Outline every Plasmodium parasite.
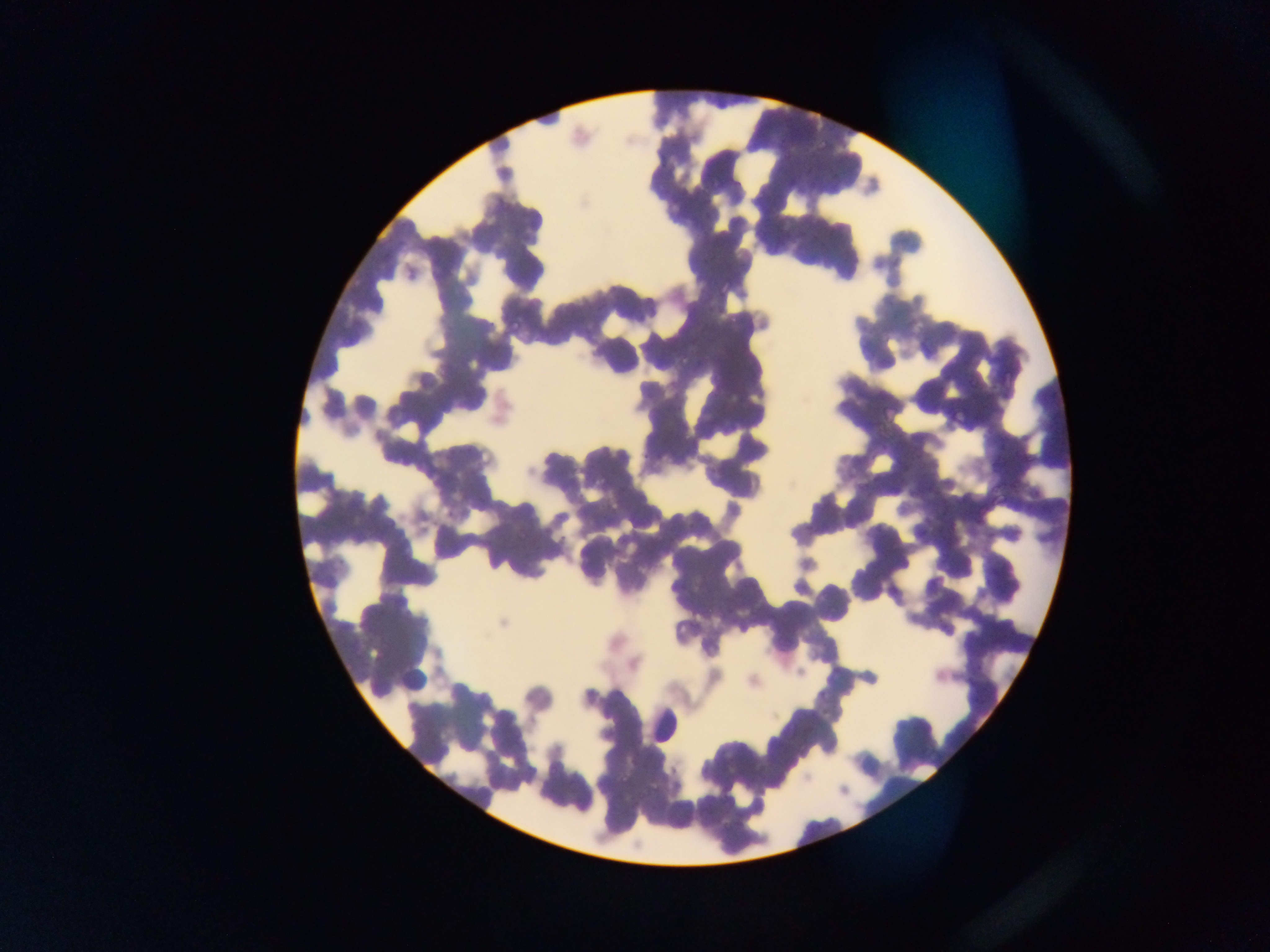

Approximate bounding boxes as [left, top, right, bottom] in pixels.
Plasmodium parasites: [816, 142, 826, 153], [825, 170, 840, 184], [829, 174, 843, 190], [706, 175, 721, 192], [826, 179, 840, 193], [648, 181, 660, 194], [717, 280, 729, 293], [724, 312, 741, 329], [509, 317, 523, 331], [948, 404, 965, 421], [513, 531, 525, 544], [619, 773, 631, 786].

preparation = thin blood smear
country = Ghana
capture = mobile-phone photograph through a microscope
image size = 1270×952 pixels
field of view = single